Name the blood parasite species.
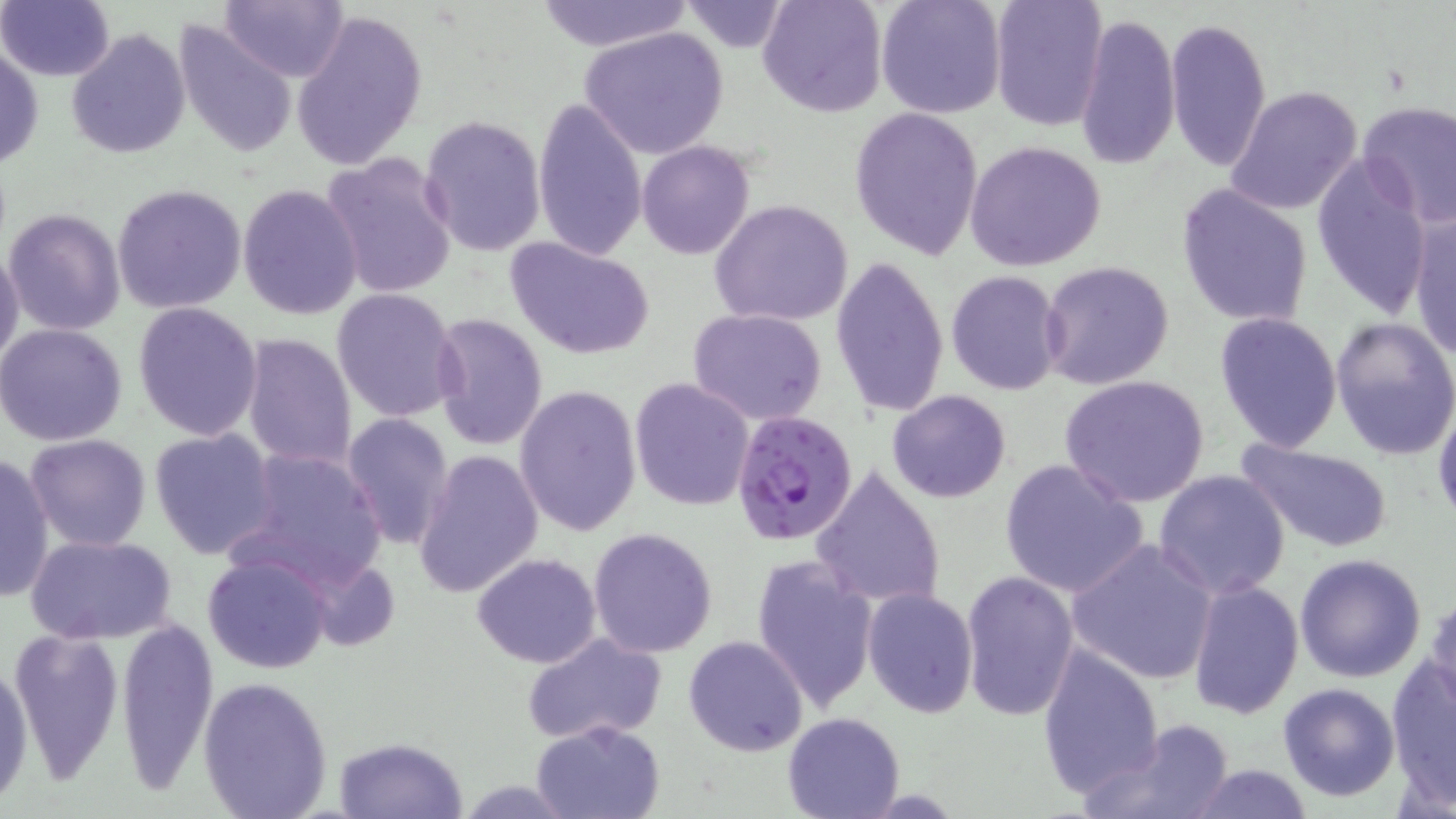
Plasmodium falciparum.

{
  "modality": "light microscopy",
  "image_size": "1456×819 pixels",
  "preparation": "thin blood film",
  "uninfected_red_blood_cell_locations": "approximate bounding boxes as (x1, y1, x2, y2) in pixels: (0, 0, 115, 82), (220, 0, 348, 83), (757, 0, 886, 117), (875, 0, 1006, 119), (990, 0, 1107, 131), (532, 1, 692, 52), (680, 2, 791, 51), (291, 9, 427, 170), (1074, 11, 1181, 172), (1164, 16, 1272, 171), (174, 20, 299, 160), (67, 27, 192, 159), (581, 27, 729, 160), (1, 42, 44, 172), (1225, 87, 1362, 215), (531, 97, 647, 261), (1357, 100, 1456, 227), (850, 104, 985, 260), (419, 114, 546, 257), (637, 140, 755, 260), (967, 140, 1106, 272), (321, 152, 458, 301), (1310, 153, 1433, 318), (237, 182, 364, 320), (112, 183, 249, 316), (1177, 183, 1313, 328), (709, 199, 853, 327), (4, 207, 125, 336), (1408, 211, 1455, 363), (505, 237, 654, 361), (0, 244, 24, 375), (830, 253, 949, 419), (1040, 260, 1174, 390), (944, 271, 1065, 396), (332, 287, 462, 423), (132, 302, 263, 441), (688, 307, 828, 425), (1214, 311, 1344, 453), (427, 312, 547, 452), (1331, 316, 1456, 461), (0, 322, 128, 447), (240, 332, 357, 471), (1061, 374, 1210, 508), (628, 376, 755, 512), (513, 383, 641, 537), (887, 389, 1013, 503), (1433, 401, 1456, 531), (341, 412, 454, 551), (149, 429, 279, 560), (25, 433, 152, 551), (1236, 437, 1394, 553), (230, 448, 388, 592), (412, 449, 545, 599), (0, 451, 53, 602), (998, 458, 1149, 599), (810, 464, 948, 610), (1154, 470, 1290, 598), (588, 527, 719, 657), (26, 534, 178, 642), (1065, 538, 1220, 685), (471, 552, 602, 669), (751, 553, 879, 713), (1293, 553, 1427, 683), (203, 554, 333, 673), (959, 570, 1081, 723), (1187, 580, 1304, 721), (862, 587, 978, 717), (1425, 595, 1456, 714), (113, 613, 220, 794), (7, 627, 125, 781), (522, 634, 666, 747), (684, 635, 810, 756), (1036, 642, 1164, 797), (0, 656, 35, 804), (1386, 657, 1456, 805), (197, 676, 334, 819), (1277, 683, 1400, 801), (782, 710, 906, 818), (1084, 719, 1235, 819), (531, 720, 664, 819), (334, 736, 469, 819), (1182, 763, 1316, 818)",
  "stain": "May-Grünwald-Giemsa",
  "plasmodium_falciparum_infected_red_blood_cell_locations": "approximate bounding boxes as (x1, y1, x2, y2) in pixels: (731, 410, 860, 547)",
  "field_of_view": "single",
  "magnification": "1000x"
}